Classify this cell by malaria status.
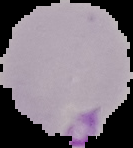
Parasitized.

Summary:
  - Image size: 133×148 pixels
  - Image type: segmented cell region on a black background
  - Preparation: thin blood film